Identify the parasite.
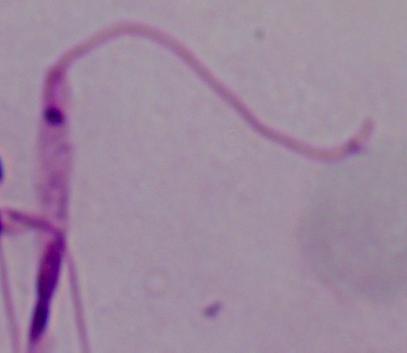

Leishmania.

Summary:
  - Magnification: 1000x
  - Modality: photomicrograph